Locate and identify every blood parasite.
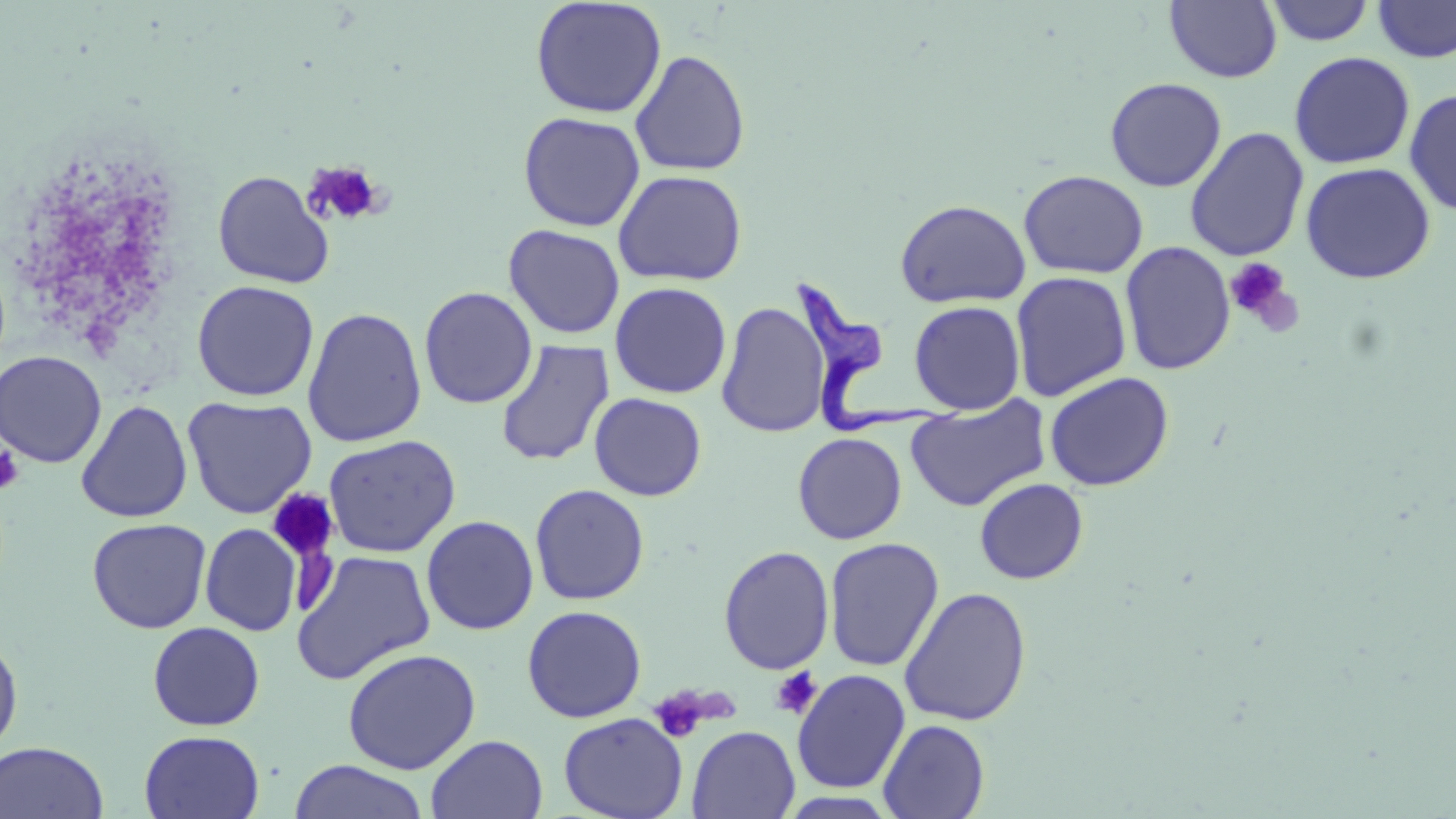
Approximate bounding boxes as (x1, y1, x2, y2) in pixels.
Trypanosoma brucei: (787, 278, 964, 438).
No Plasmodium falciparum, Plasmodium ovale, Plasmodium malariae, Plasmodium vivax, or Babesia divergens observed.

Summary:
  - Uninfected red blood cell locations: (530, 0, 667, 118), (1165, 1, 1282, 83), (1263, 1, 1376, 46), (1372, 1, 1456, 63), (630, 49, 751, 177), (1288, 51, 1416, 170), (1105, 77, 1227, 192), (1404, 88, 1456, 216), (518, 111, 646, 232), (1185, 126, 1310, 262), (1300, 161, 1435, 284), (612, 169, 748, 286), (1018, 169, 1148, 279), (213, 170, 336, 289), (894, 198, 1031, 308), (503, 224, 625, 340), (1120, 240, 1236, 375), (1010, 270, 1132, 402), (192, 279, 319, 401), (609, 282, 732, 399), (419, 287, 538, 409), (715, 300, 831, 438), (909, 300, 1026, 414), (302, 307, 427, 447), (495, 339, 615, 467), (0, 350, 107, 468), (1044, 371, 1174, 491), (589, 392, 707, 501), (906, 395, 1050, 511), (182, 396, 317, 519), (75, 399, 193, 523), (793, 432, 907, 544), (324, 434, 461, 558), (974, 478, 1089, 584), (529, 483, 650, 605), (421, 515, 539, 636), (87, 518, 211, 633), (200, 523, 302, 636), (823, 537, 945, 672), (718, 545, 835, 675), (290, 550, 436, 685), (898, 586, 1032, 727), (522, 605, 646, 723), (147, 621, 265, 731), (0, 632, 23, 757), (342, 647, 481, 775), (791, 669, 911, 793), (558, 712, 687, 819), (878, 719, 990, 819), (686, 725, 800, 818), (139, 729, 265, 819), (426, 734, 548, 819), (0, 741, 109, 819), (288, 760, 429, 819)
  - Platelet locations: (303, 161, 384, 226), (1225, 258, 1294, 326), (0, 444, 24, 494), (266, 490, 339, 563), (770, 667, 822, 719), (654, 685, 708, 745)
  - Slide-level diagnosis: Trypanosoma brucei
  - Field of view: one of a larger specimen
  - Preparation: thin blood film
  - Magnification: 1000x
  - Image size: 1456×819 pixels
  - Stain: May-Grünwald-Giemsa
  - Modality: light microscopy